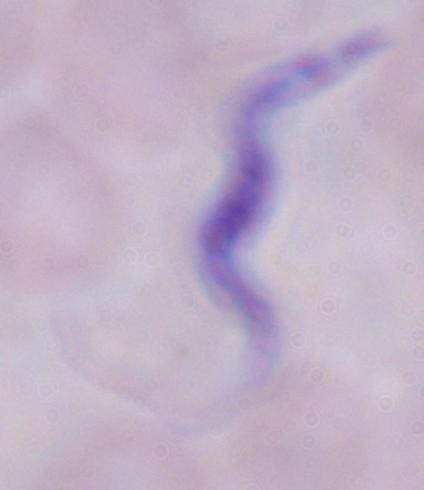

magnification = 1000x
modality = micrograph
identification = trypanosome